Comment on the morphology of the erythrocytes.
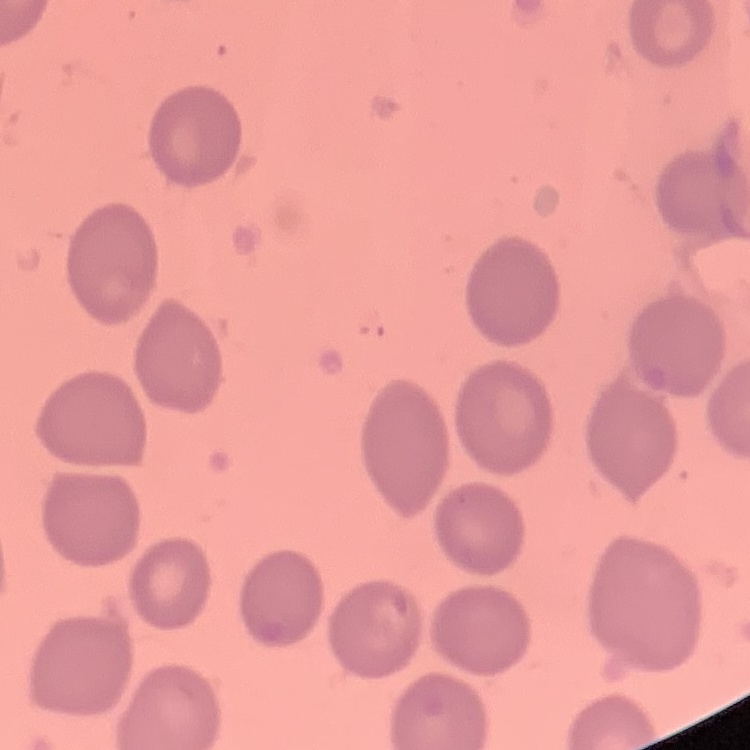

They show no rouleaux formation.

One tile cut from a larger photomicrograph. Thin blood film. Stained with either Field's or Giemsa.